Give the position of every Plasmodium parasite visible.
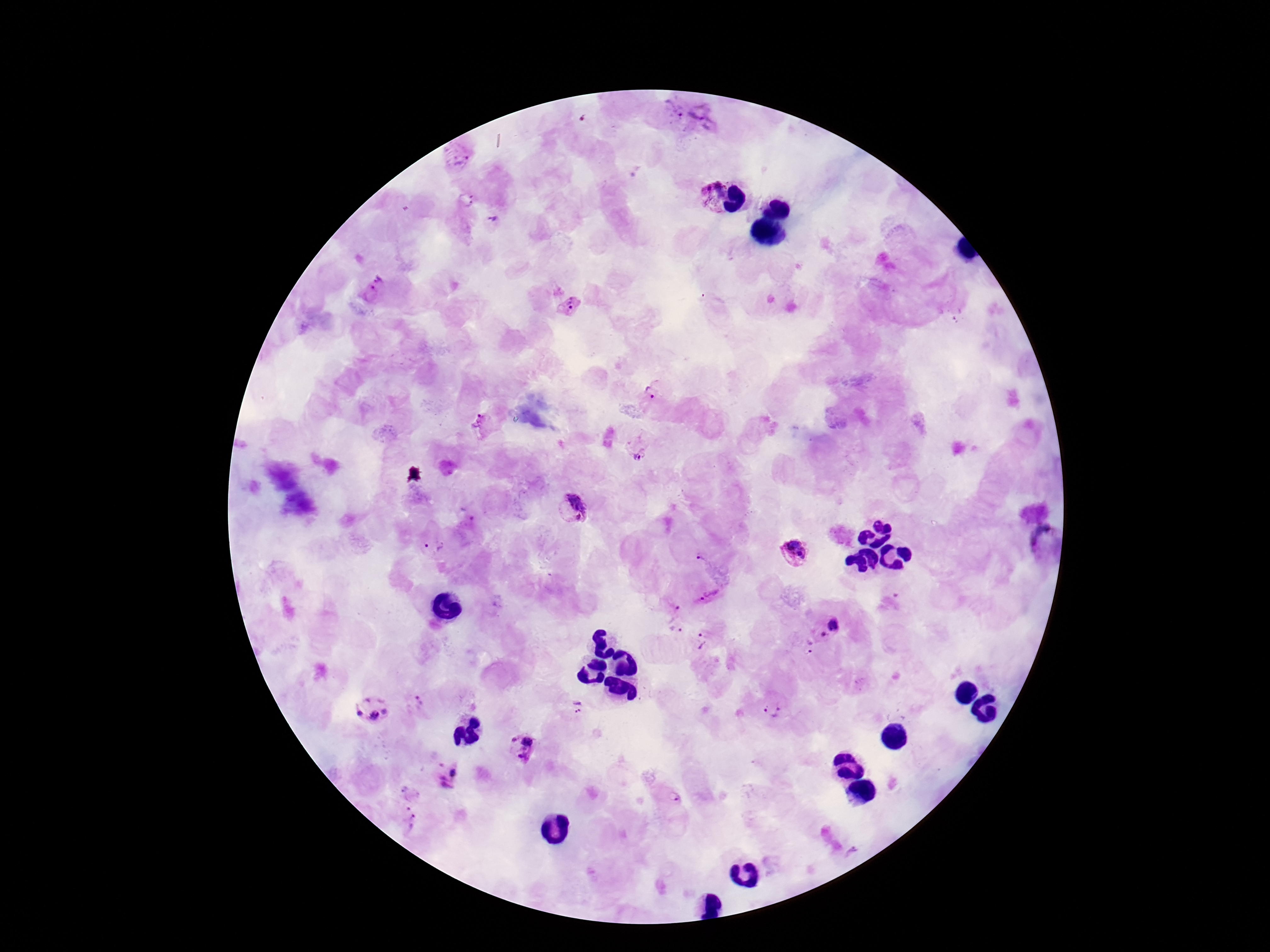

Approximate centers as {x, y} in pixels.
Plasmodium parasites: {675, 114}, {703, 116}, {457, 156}, {711, 194}, {467, 201}, {495, 224}, {374, 292}, {569, 305}, {649, 392}, {483, 424}, {638, 447}, {571, 509}, {1045, 541}, {435, 546}, {794, 550}, {705, 558}, {709, 596}, {671, 607}, {827, 626}, {676, 629}, {702, 639}, {807, 647}, {417, 703}, {771, 703}, {579, 707}, {372, 709}, {522, 747}, {446, 776}, {670, 796}, {404, 820}.

{
  "capture": "smartphone camera through the microscope eyepiece",
  "preparation": "thick peripheral-blood smear",
  "magnification": "100x",
  "image_size": "1270×952 pixels",
  "patient_malaria_status": "positive",
  "stain": "Giemsa",
  "field_of_view": "one from this slide"
}